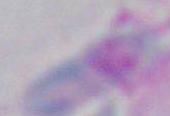

Summary:
  - Identification: Toxoplasma gondii
  - Magnification: 1000x
  - Modality: micrograph